Assess this cell for malaria.
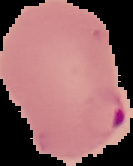
Parasitized.

Summary:
  - Preparation: thin blood film
  - Image size: 133×166 pixels
  - Image type: cell region segmented out of the field of view; surrounding area masked to black